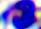 A white blood cell is seen. Micrograph. 400x magnification.